Report the malaria status of this cell.
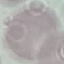
It is uninfected.

stain = Giemsa
preparation = thin blood film
capture = smartphone camera at the microscope eyepiece
image type = automatically extracted cell patch, resized to 64 × 64 pixels